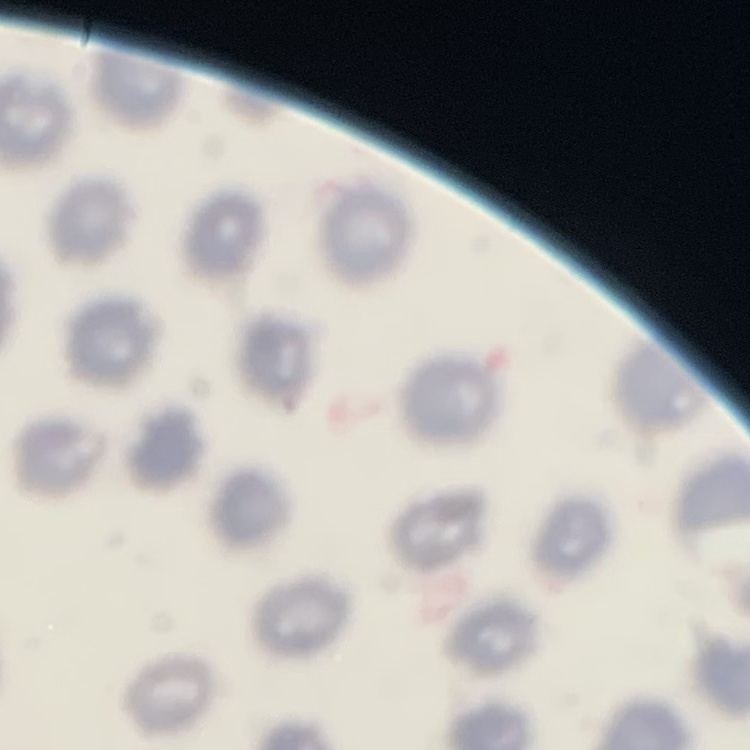

erythrocyte morphology = no rouleaux formation
stain = Field's or Giemsa
preparation = thin peripheral smear
image type = square crop of a larger photomicrograph